Give the position of every Plasmodium parasite.
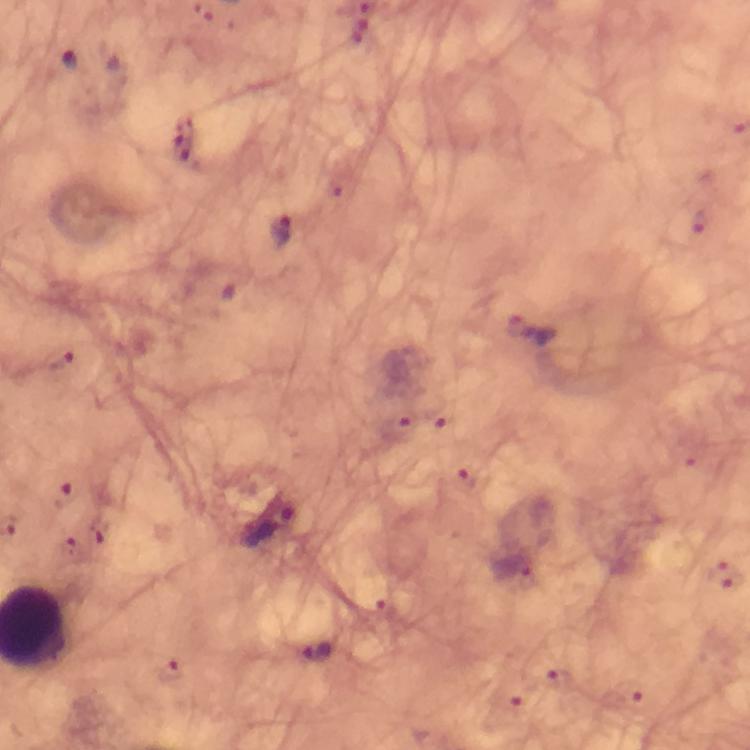

Approximate centers as {x, y} in pixels.
Plasmodium parasites: {182, 146}, {700, 222}, {283, 230}, {519, 325}, {438, 419}, {401, 424}, {466, 481}, {65, 496}, {511, 567}, {317, 652}, {169, 671}.

cropped from = one field of view
image size = 750×750 pixels
stain = Giemsa
magnification = 100x
capture = smartphone camera through the microscope
preparation = thick smear
context = from a malaria diagnostic workup
immersion oil = used